Report the malaria status.
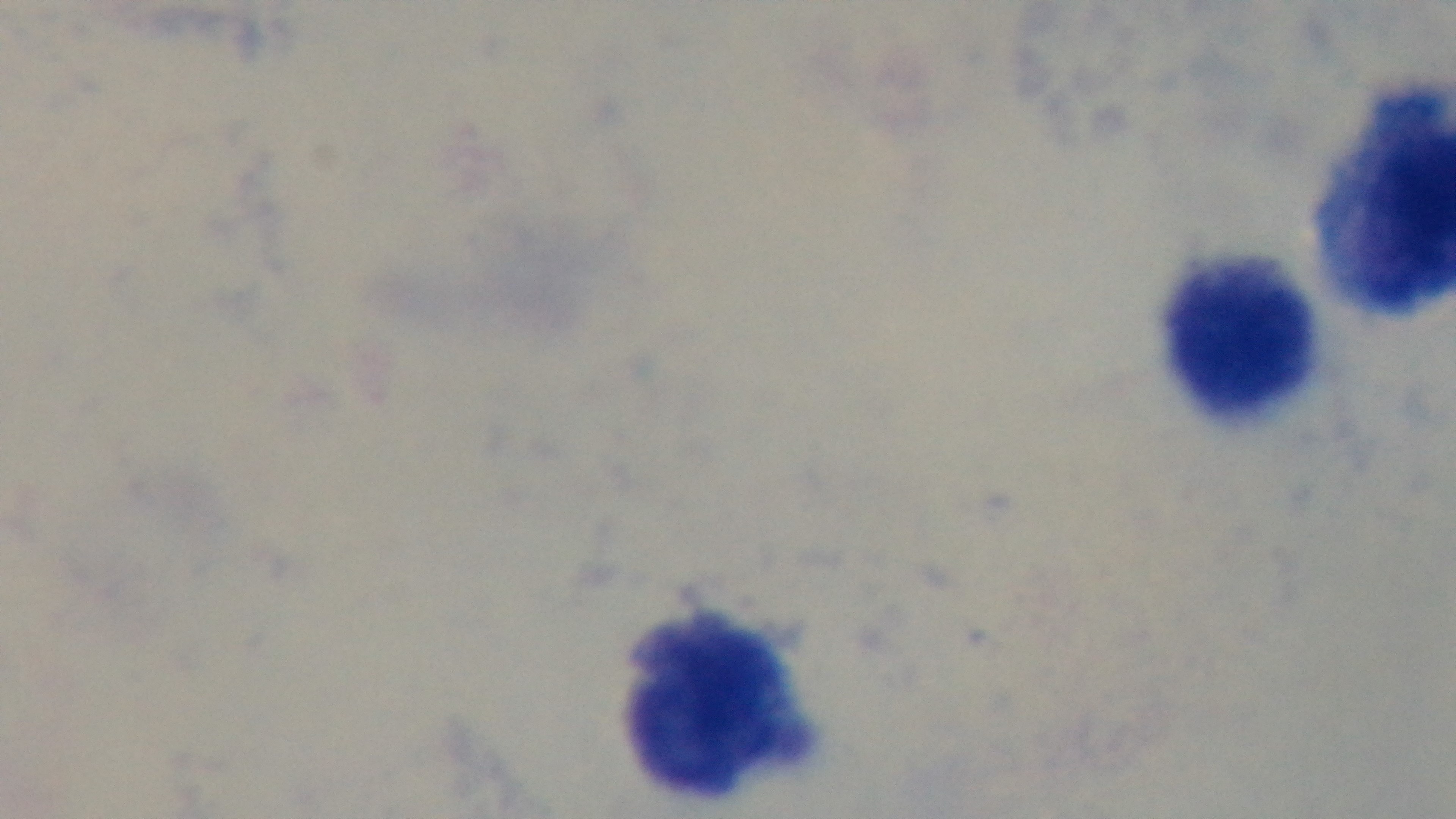
Negative.

Summary:
  - Objective: 100x oil immersion
  - Preparation: thick blood film
  - Capture: mounted 4K digital camera
  - Field of view: one from the slide
  - Modality: light microscopy
  - Stain: Giemsa